Report the malaria status of this cell.
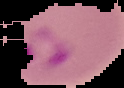
Parasitized.

From a thin blood smear. Cell region segmented out of the field of view; the surrounding area is masked to black. Image is 124×88 pixels.